State which parasite is depicted.
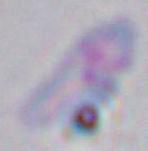

Toxoplasma gondii.

Summary:
  - Magnification: 1000x
  - Modality: photomicrograph